Classify this cell by malaria status.
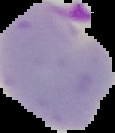
Parasitized.

Summary:
  - Image size: 115×133 pixels
  - Image type: cell region segmented out of the field of view; surrounding area masked to black
  - Preparation: thin blood smear